Classify this cell by malaria status.
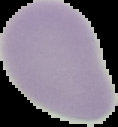
It is uninfected.

Summary:
  - Preparation: thin blood smear
  - Image type: segmented cell region with the area outside set to black
  - Image size: 118×127 pixels